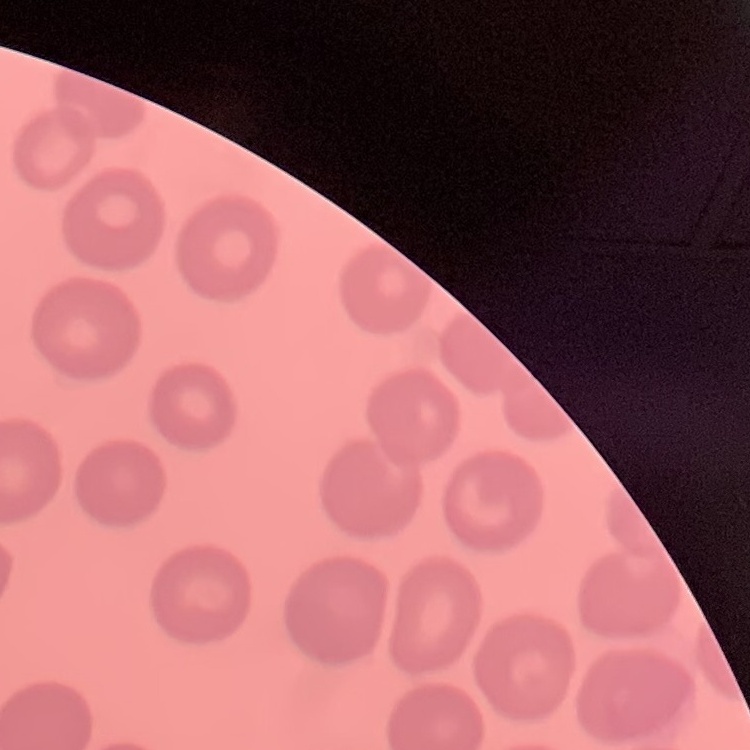

Summary:
  - Red blood cell morphology: no rouleaux formation
  - Preparation: thin blood smear
  - Image type: one tile cut from a larger photomicrograph
  - Stain: Field's or Giemsa